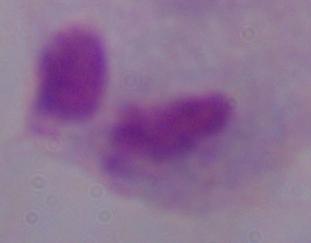
identification = trichomonad
modality = photomicrograph
magnification = 1000x